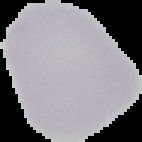
Image is 142×142 pixels. From a thin blood smear. Result: no malaria parasites detected. Segmented cell region on a black background.